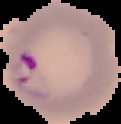
image size = 121×124 pixels
result = Plasmodium parasites identified
preparation = thin blood film
image type = segmented cell region with the area outside set to black